Point out each leukocyte.
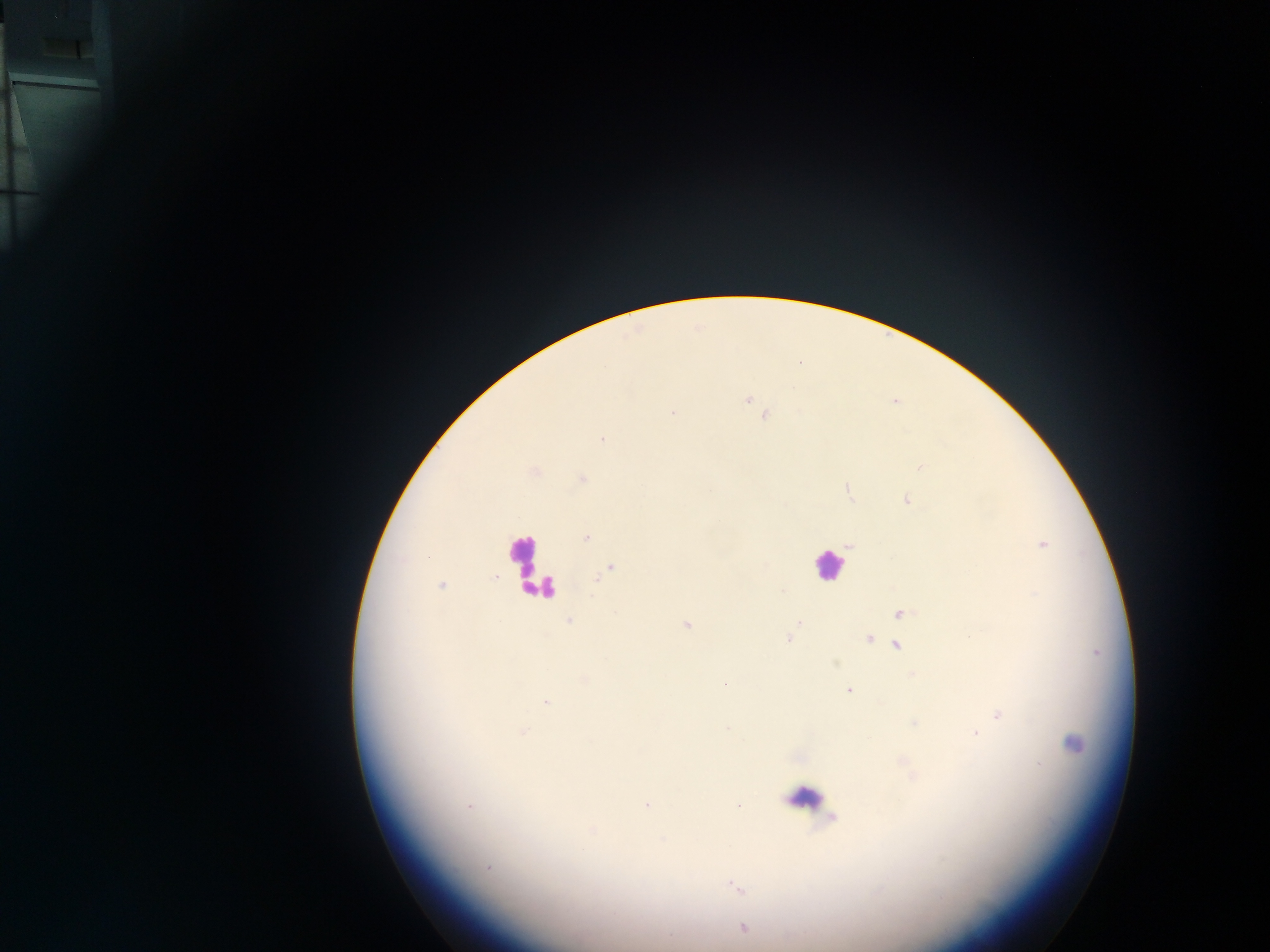
Approximate centers as (x, y) in pixels.
Leukocytes: (523, 557), (827, 565), (538, 585), (810, 800).

Summary:
  - Malaria parasite locations: (748, 399), (894, 402), (673, 413), (765, 415), (601, 439), (920, 467), (535, 473), (582, 478), (848, 491), (907, 500), (586, 538), (1043, 544), (849, 545), (609, 569), (441, 585), (1035, 595), (901, 613), (568, 621), (798, 623), (687, 625), (788, 638), (869, 638), (898, 645), (725, 684), (848, 690), (546, 702), (998, 714), (915, 723), (727, 728), (523, 732), (976, 734), (1073, 744), (1039, 764), (647, 805), (737, 806), (470, 807), (591, 831), (488, 868), (737, 888), (743, 928), (670, 936)
  - Country: Ghana
  - Preparation: thick blood film
  - Capture: mobile-phone photograph through a microscope
  - Field of view: single
  - Image size: 1270×952 pixels